Locate every malaria parasite.
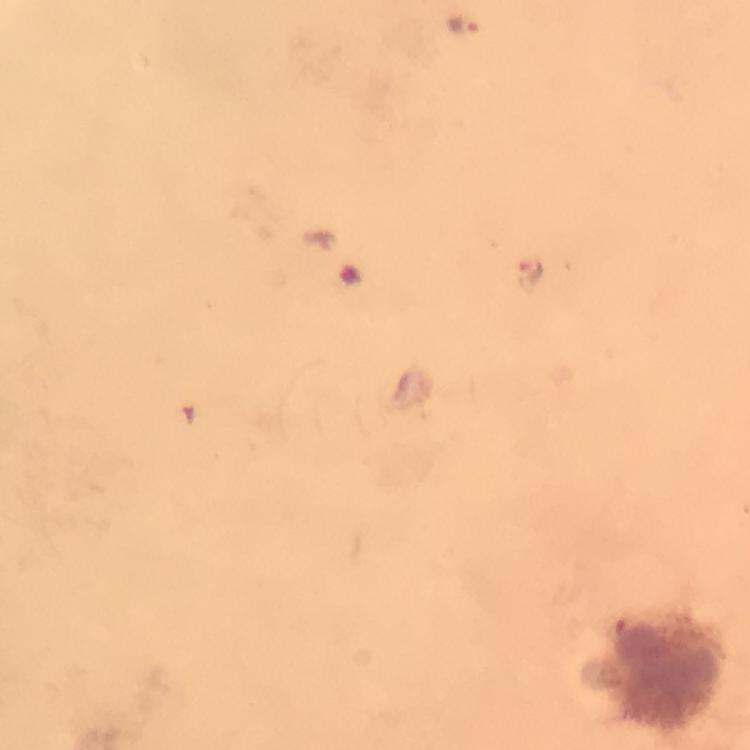

Approximate centers as {x, y} in pixels.
Malaria parasites: {464, 26}.

immersion oil = applied
cropped from = one field of view
stain = Giemsa
image size = 750×750 pixels
preparation = thick blood smear
magnification = 100x
leukocyte locations = approximate centers as {x, y} in pixels: {667, 675}
capture = smartphone mounted on the microscope
context = from a malaria diagnostic workup